Assess the morphology of the red blood cells.
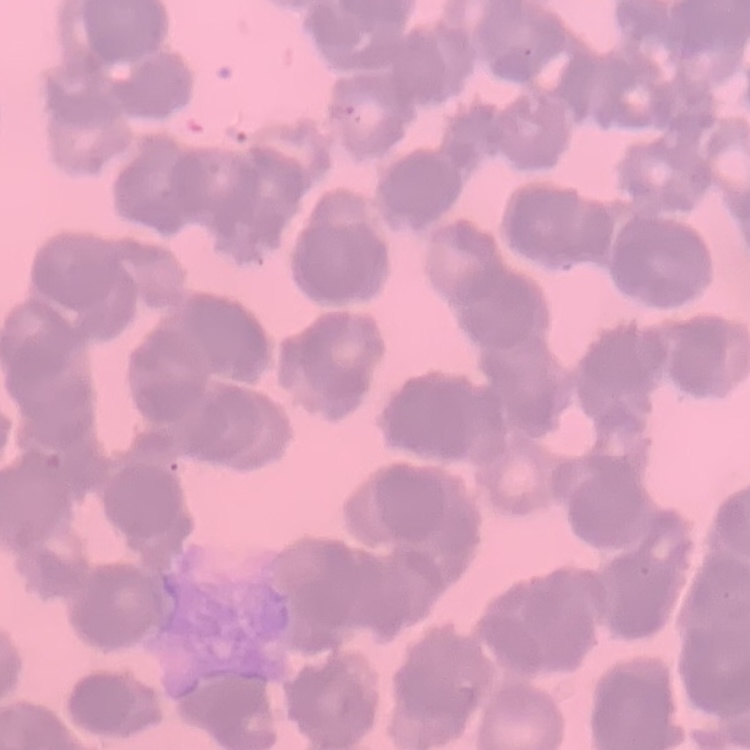

Rouleaux formation.

Summary:
  - Stain: Field's or Giemsa
  - Image type: square crop of a larger photomicrograph
  - Preparation: thin blood smear